State which parasite is depicted.
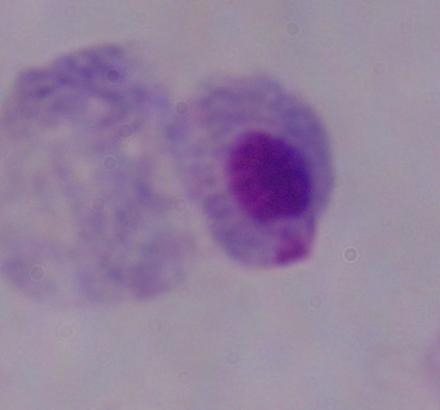

This is a trichomonad.

Summary:
  - Modality: photomicrograph
  - Magnification: 1000x